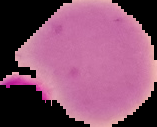

Summary:
  - Result: negative for Plasmodium parasites
  - Image type: segmented cell region with the area outside set to black
  - Preparation: thin blood film
  - Image size: 157×127 pixels